Assess the morphology of the erythrocytes.
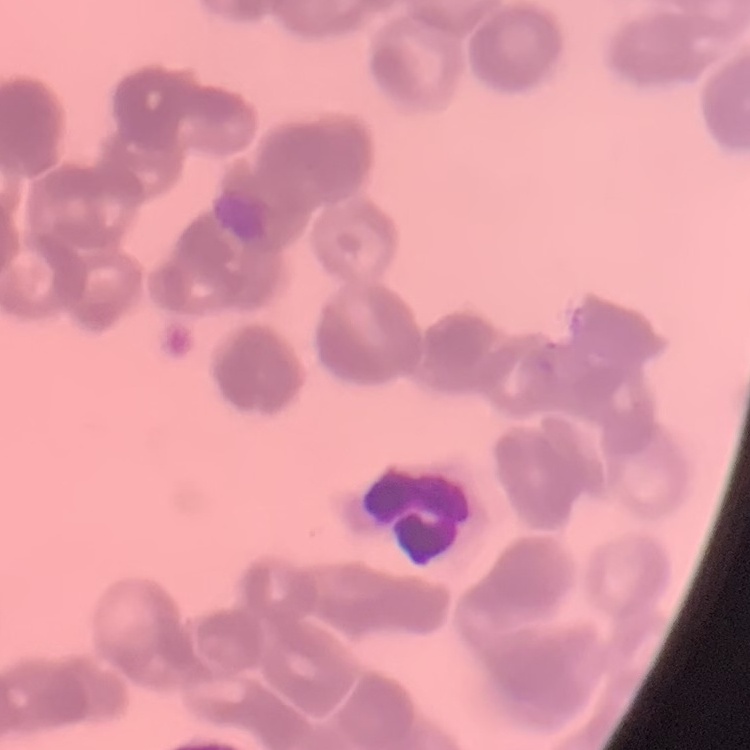

They show rouleaux formation.

Summary:
  - Image type: square crop of a larger photomicrograph
  - Stain: Field's or Giemsa
  - Preparation: thin blood smear